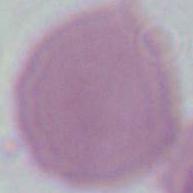

modality: micrograph
identification: erythrocyte
magnification: 1000x